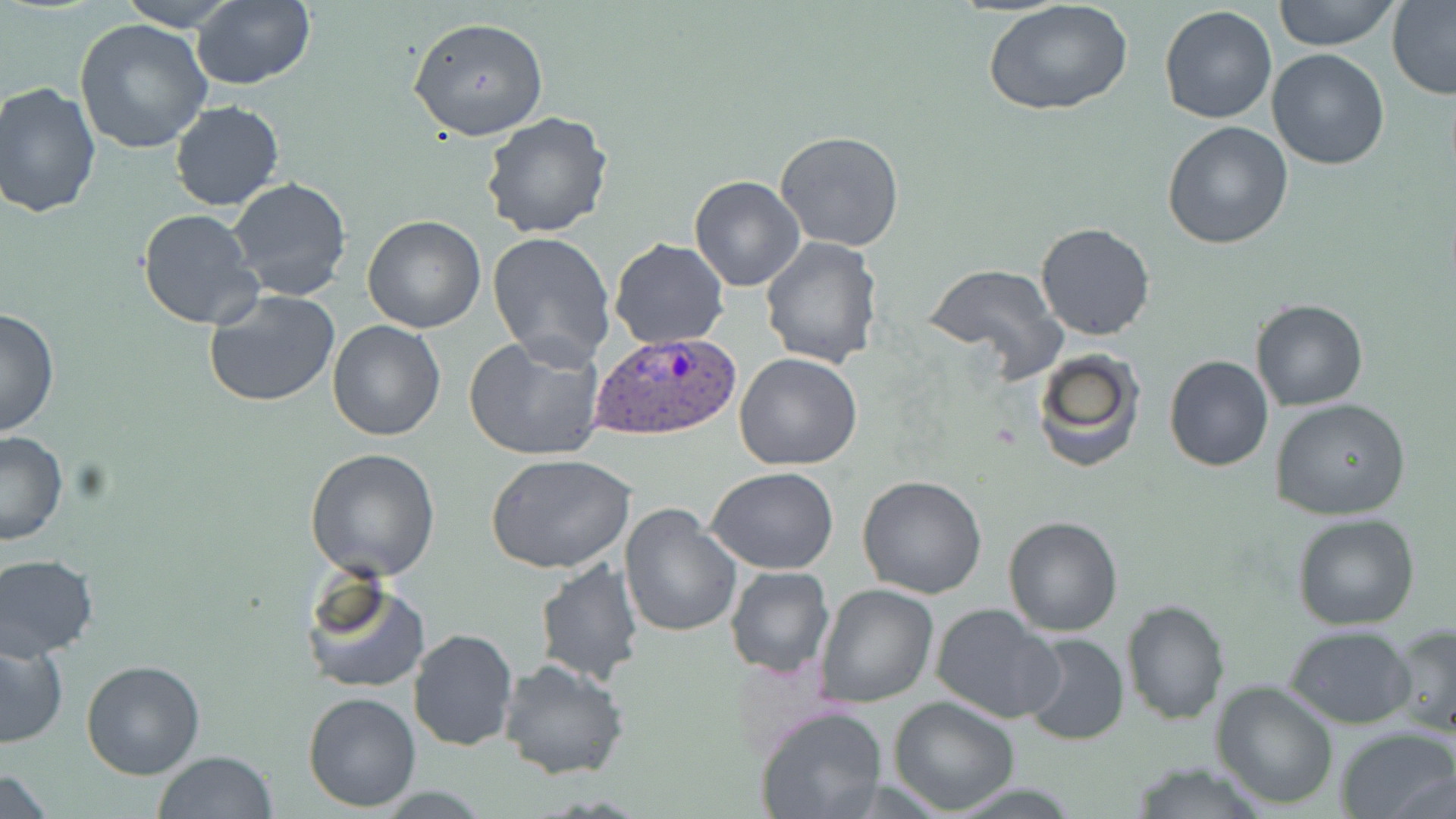

slide-level diagnosis = Plasmodium ovale
stain = May-Grünwald-Giemsa
magnification = 1000x
modality = optical microscopy
field of view = one of a larger specimen
preparation = thin blood film
uninfected red blood cell locations = approximate bounding boxes as (x1,y1)-(x2,y2) corner pairs in pixels: (120,0)-(239,29), (1272,0)-(1401,51), (190,1)-(315,91), (1387,1)-(1456,101), (985,2)-(1134,118), (1159,4)-(1278,126), (408,17)-(550,141), (74,18)-(213,156), (1267,48)-(1391,170), (0,82)-(102,219), (170,101)-(285,212), (479,111)-(613,240), (1162,121)-(1294,249), (774,130)-(905,252), (689,174)-(806,291), (226,177)-(352,303), (137,208)-(263,329), (361,214)-(487,332), (1035,222)-(1156,341), (487,230)-(617,367), (760,236)-(882,368), (608,239)-(727,350), (923,262)-(1064,372), (204,289)-(341,408), (1249,298)-(1368,411), (0,306)-(59,438), (327,319)-(447,440), (463,333)-(607,462), (1031,348)-(1145,473), (734,352)-(863,472), (1164,355)-(1273,472), (1270,398)-(1411,521), (0,431)-(70,548), (304,446)-(442,581), (485,453)-(637,574), (707,467)-(840,575), (857,475)-(987,598), (618,504)-(742,636), (1292,514)-(1421,629), (1003,516)-(1123,636), (0,554)-(99,660), (534,557)-(646,685), (725,565)-(834,679), (300,575)-(431,694), (814,583)-(940,707), (1121,598)-(1228,723), (929,603)-(1063,724), (1386,623)-(1455,738), (1286,626)-(1415,729), (408,628)-(518,752), (1019,633)-(1129,746), (0,634)-(70,748), (498,657)-(630,781), (79,660)-(205,778), (1211,680)-(1339,808), (301,692)-(421,812), (888,696)-(1020,814), (754,706)-(887,819), (1335,726)-(1456,819), (152,750)-(277,819), (1125,761)-(1270,817), (2,771)-(57,819)
image size = 1456×819 pixels
Plasmodium ovale-infected red blood cell locations = approximate bounding boxes as (x1,y1)-(x2,y2) corner pairs in pixels: (589,330)-(739,440)